Locate platelets.
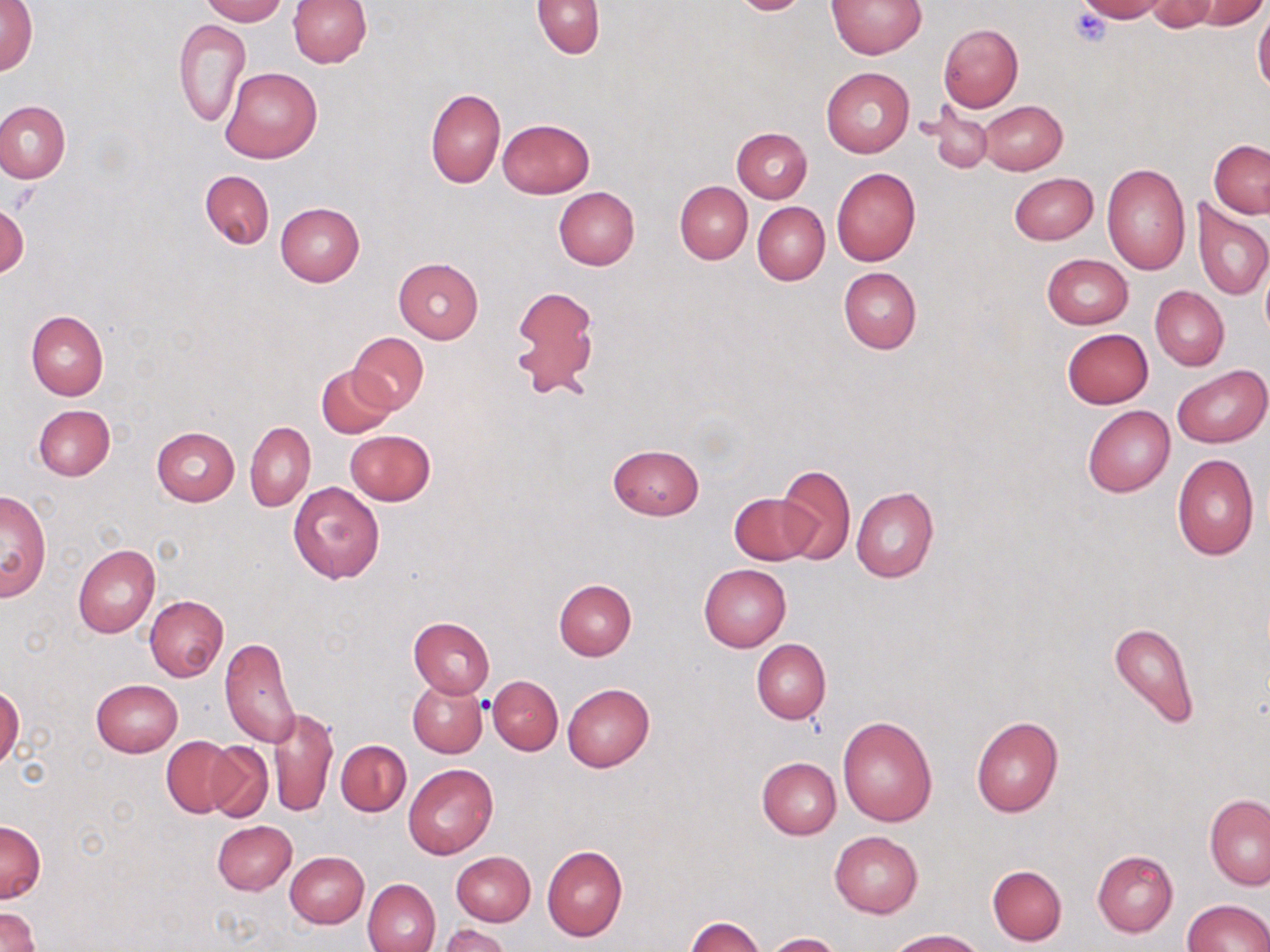
Approximate bounding boxes as (x1,y1)-(x2,y2) corner pairs in pixels.
Platelets: (1068,7)-(1114,47).

Uninfected red blood cell locations: (1,0)-(37,77), (201,0)-(286,24), (287,0)-(370,68), (826,0)-(927,58), (1074,0)-(1168,22), (533,1)-(604,58), (1145,1)-(1221,32), (1192,1)-(1269,29), (1253,6)-(1270,94), (174,18)-(250,126), (937,22)-(1023,112), (220,66)-(323,164), (821,68)-(914,158), (426,88)-(505,188), (0,99)-(70,183), (980,101)-(1067,174), (924,105)-(995,174), (498,118)-(594,197), (732,127)-(812,202), (1209,140)-(1270,217), (1102,162)-(1191,275), (832,168)-(922,267), (200,170)-(274,250), (1008,172)-(1098,246), (675,181)-(752,262), (553,186)-(640,269), (1192,199)-(1269,302), (0,202)-(28,279), (752,202)-(829,285), (275,203)-(365,286), (1042,253)-(1133,329), (394,258)-(485,344), (1260,258)-(1269,347), (838,267)-(922,354), (508,285)-(600,400), (1150,286)-(1228,371), (27,311)-(108,399), (1062,329)-(1153,408), (348,332)-(429,413), (1172,364)-(1269,448), (316,366)-(395,437), (34,404)-(115,480), (1082,404)-(1176,497), (245,421)-(315,511), (150,427)-(240,505), (345,430)-(435,505), (608,443)-(704,519), (1172,453)-(1259,559), (777,465)-(855,564), (289,482)-(385,583), (851,487)-(938,583), (0,491)-(52,600), (731,492)-(817,565), (72,544)-(159,638), (699,563)-(791,651), (554,579)-(636,661), (146,595)-(227,681), (408,616)-(495,697), (1108,620)-(1199,728), (220,638)-(301,747), (751,639)-(830,724), (489,675)-(563,755), (91,679)-(183,757), (408,680)-(487,757), (562,683)-(654,771), (0,686)-(24,770), (269,707)-(336,817), (837,715)-(936,826), (971,715)-(1063,817), (163,737)-(236,816), (337,740)-(411,817), (203,742)-(275,822), (757,756)-(840,839), (403,764)-(497,859), (1204,794)-(1270,889), (212,819)-(297,896), (0,820)-(45,903), (830,831)-(923,917), (542,844)-(628,940), (1092,850)-(1179,937), (284,851)-(368,928), (452,851)-(535,925), (987,864)-(1067,946), (363,877)-(441,951), (1182,899)-(1270,951), (0,907)-(41,952), (687,917)-(765,952), (439,923)-(513,951), (887,929)-(983,951), (765,932)-(841,952). Slide-level diagnosis: negative for blood parasites. May-Grünwald-Giemsa-stained preparation. Single field of view. Thin blood smear. Light microscopy. Captured at 1000x magnification. Image is 1270×952 pixels.